Report the malaria status of this cell.
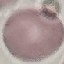
Uninfected.

{
  "stain": "Giemsa",
  "image_type": "cell patch, automatically extracted from a larger field of view and resized to 64 × 64 pixels",
  "preparation": "thin smear",
  "capture": "smartphone camera at the microscope eyepiece"
}